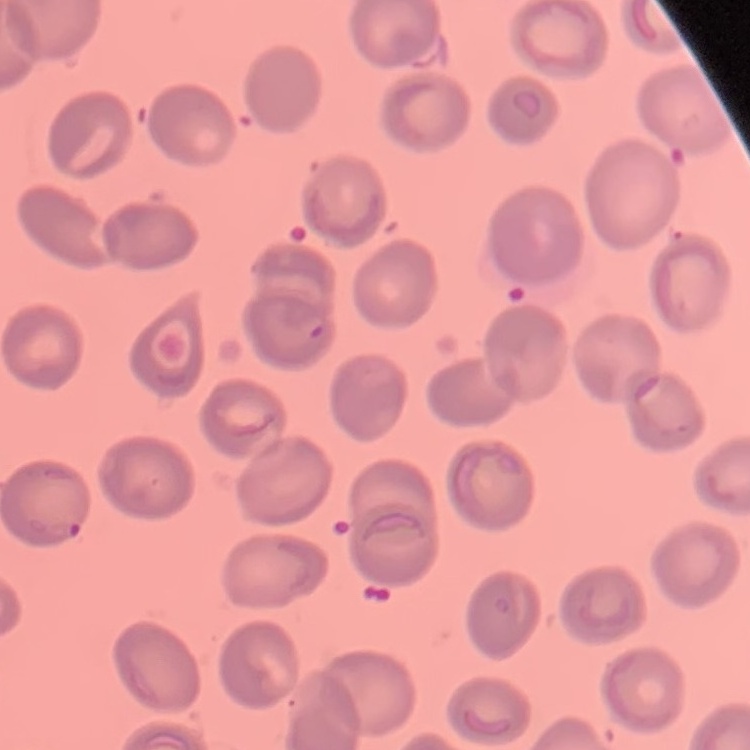

Summary:
  - Red blood cell morphology: no rouleaux formation
  - Stain: Field's or Giemsa
  - Preparation: thin peripheral smear
  - Image type: one tile cut from a larger photomicrograph